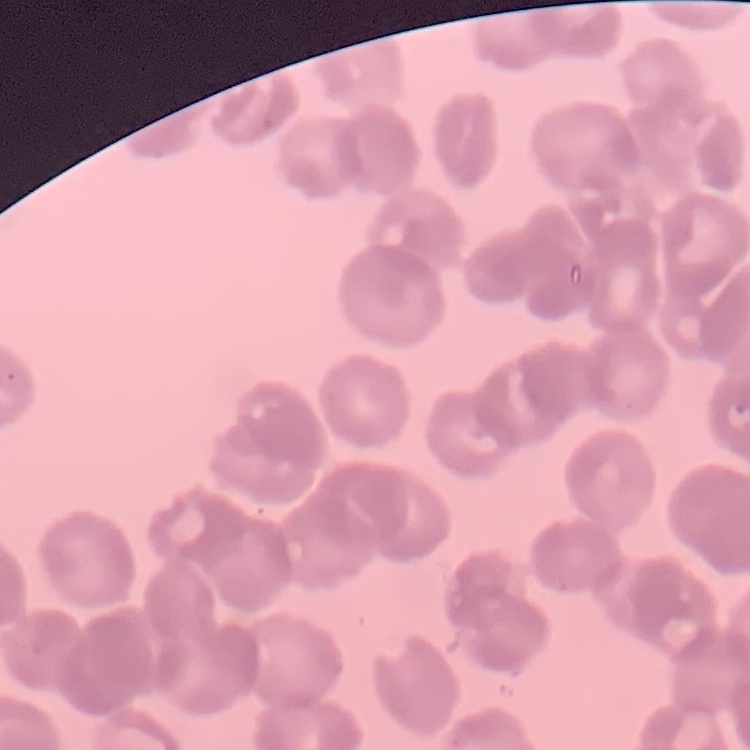
The red blood cells exhibit rouleaux formation. Field's or Giemsa stain. Square crop of a larger photomicrograph. Thin blood smear.